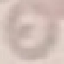

Malaria status: uninfected. Giemsa stain. Thin smear of blood. Acquired by smartphone through the microscope eyepiece. Automatically extracted cell patch, resized to 64 × 64 pixels.